Outline each Plasmodium falciparum parasite and classify it by life-cycle stage.
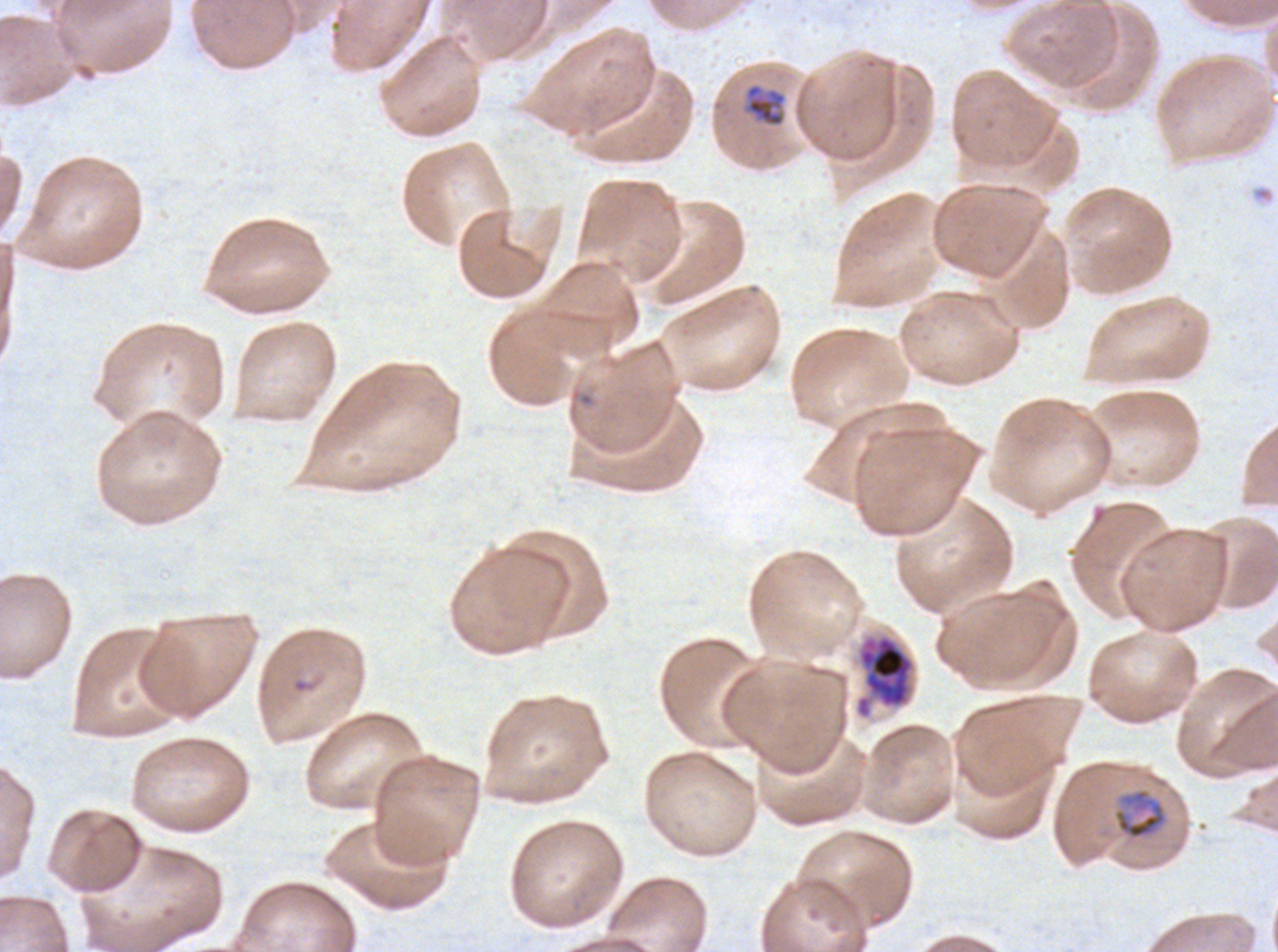

Approximate bounding boxes as {x1, y1, x2, y2} in pixels.
Late-ring/early-trophozoite forms: {743, 82, 787, 128}.
Mid trophozoites: {1112, 787, 1169, 841}.
Early schizonts: {854, 632, 916, 720}.
No rings, late trophozoites, late schizonts, segmenters, or gametocytes observed.

debris locations = {1251, 185, 1275, 203}
preparation = thin blood smear
image size = 1278×952 pixels
specimen = Plasmodium falciparum from a patient in The Gambia, cultured ex vivo for 24 to 48 hours
stain = Giemsa
life-cycle stages observed = late-ring/early-trophozoite, mid trophozoite, early schizont
field of view = one sub-image of a larger composite